Assess this cell for malaria.
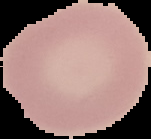

Uninfected.

Summary:
  - Preparation: thin blood film
  - Image type: segmented cell region with the area outside set to black
  - Image size: 151×139 pixels